Describe the morphology of the red blood cells.
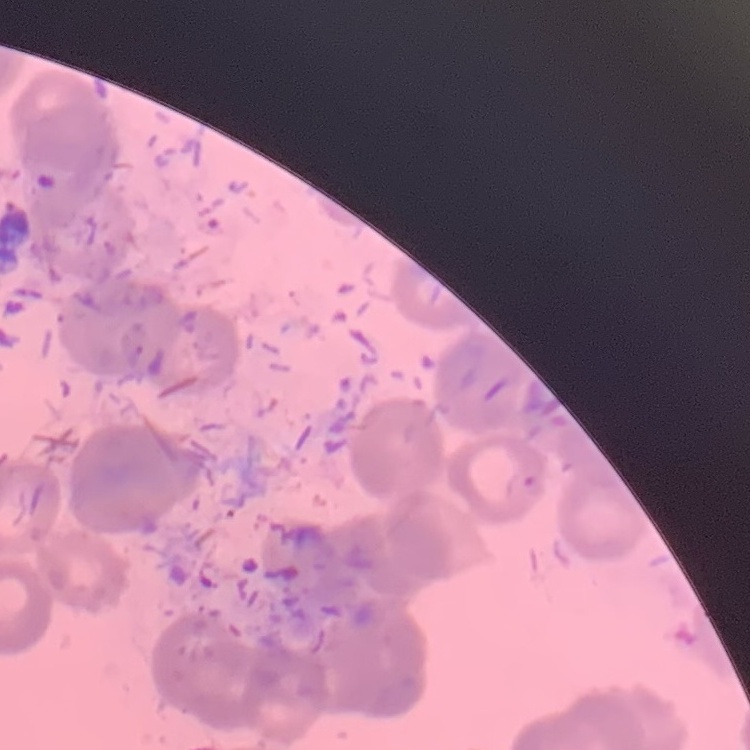

They show rouleaux formation.

Summary:
  - Image type: one tile cut from a larger photomicrograph
  - Stain: Field's or Giemsa
  - Preparation: thin peripheral smear